Outline each uninfected red blood cell.
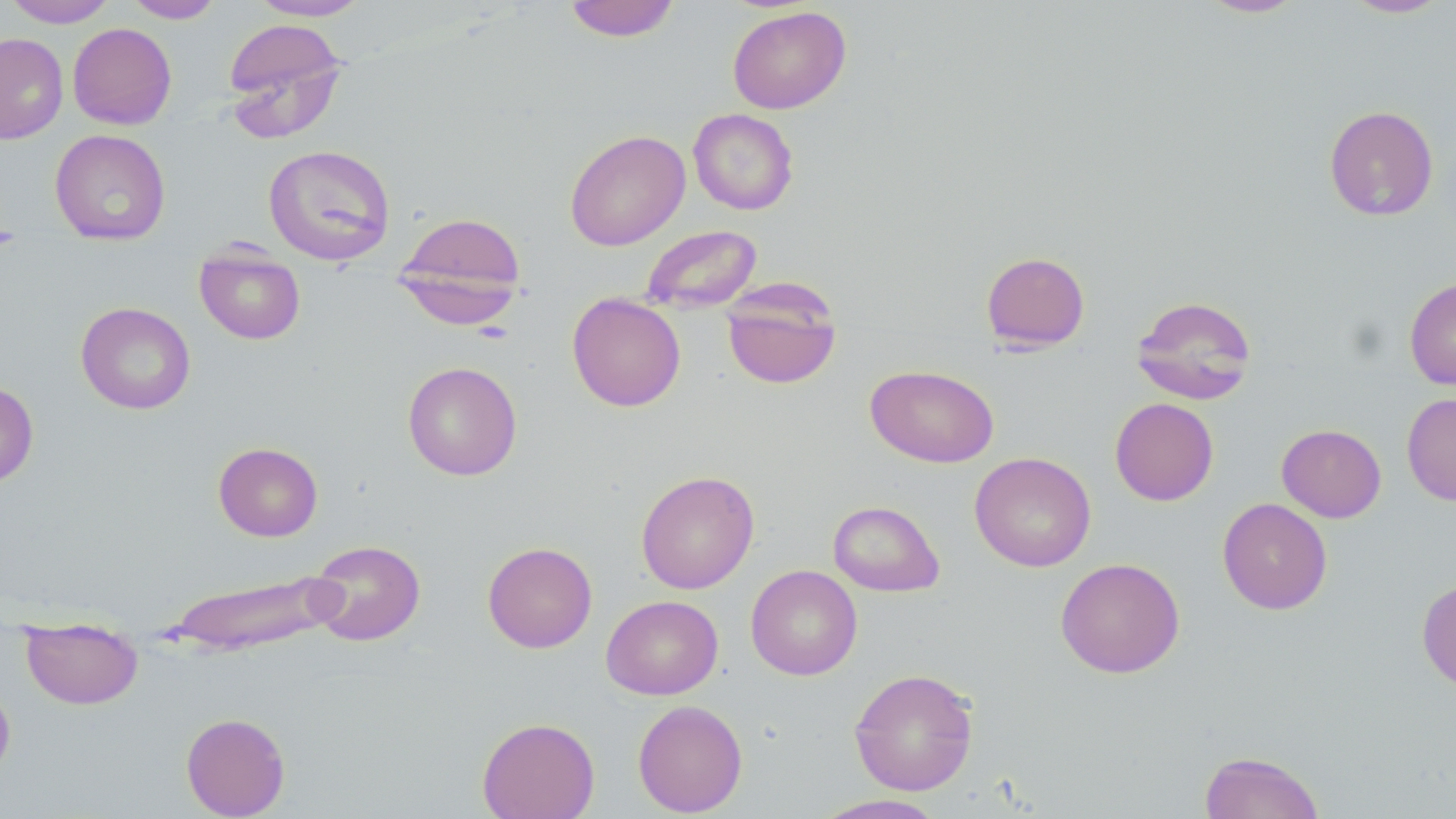

Approximate bounding boxes as named x1/y1/x2/y2 corners in pixels.
Uninfected red blood cells: (x1=3, y1=0, x2=119, y2=27), (x1=123, y1=0, x2=224, y2=23), (x1=248, y1=0, x2=372, y2=21), (x1=563, y1=0, x2=680, y2=42), (x1=1196, y1=0, x2=1308, y2=18), (x1=1340, y1=0, x2=1451, y2=19), (x1=727, y1=6, x2=851, y2=114), (x1=222, y1=18, x2=348, y2=141), (x1=68, y1=23, x2=177, y2=129), (x1=0, y1=33, x2=68, y2=144), (x1=1323, y1=105, x2=1439, y2=221), (x1=688, y1=109, x2=799, y2=214), (x1=50, y1=129, x2=171, y2=245), (x1=565, y1=130, x2=690, y2=251), (x1=262, y1=144, x2=396, y2=266), (x1=394, y1=211, x2=527, y2=319), (x1=639, y1=224, x2=764, y2=314), (x1=194, y1=245, x2=305, y2=344), (x1=981, y1=251, x2=1090, y2=352), (x1=1404, y1=276, x2=1456, y2=390), (x1=721, y1=280, x2=842, y2=390), (x1=567, y1=292, x2=686, y2=412), (x1=1130, y1=295, x2=1257, y2=405), (x1=76, y1=302, x2=195, y2=414), (x1=402, y1=361, x2=522, y2=480), (x1=866, y1=364, x2=999, y2=468), (x1=0, y1=379, x2=38, y2=489), (x1=1401, y1=393, x2=1456, y2=506), (x1=1110, y1=398, x2=1218, y2=506), (x1=1276, y1=424, x2=1387, y2=523), (x1=213, y1=442, x2=323, y2=541), (x1=969, y1=452, x2=1096, y2=571), (x1=635, y1=470, x2=760, y2=594), (x1=1217, y1=497, x2=1333, y2=615), (x1=828, y1=500, x2=944, y2=596), (x1=307, y1=539, x2=426, y2=646), (x1=482, y1=541, x2=597, y2=653), (x1=1055, y1=557, x2=1185, y2=678), (x1=745, y1=564, x2=863, y2=680), (x1=160, y1=570, x2=345, y2=657), (x1=1416, y1=578, x2=1456, y2=692), (x1=601, y1=595, x2=723, y2=700), (x1=21, y1=619, x2=143, y2=710), (x1=849, y1=667, x2=979, y2=796), (x1=0, y1=679, x2=15, y2=785), (x1=632, y1=699, x2=747, y2=817), (x1=180, y1=712, x2=290, y2=818), (x1=477, y1=717, x2=600, y2=819), (x1=1198, y1=751, x2=1325, y2=818), (x1=810, y1=794, x2=950, y2=818).

slide_level_diagnosis: no evidence of blood parasites
image_size: 1456×819 pixels
preparation: thin blood smear
stain: May-Grünwald-Giemsa
modality: optical microscopy
field_of_view: one of a larger specimen
magnification: 1000x